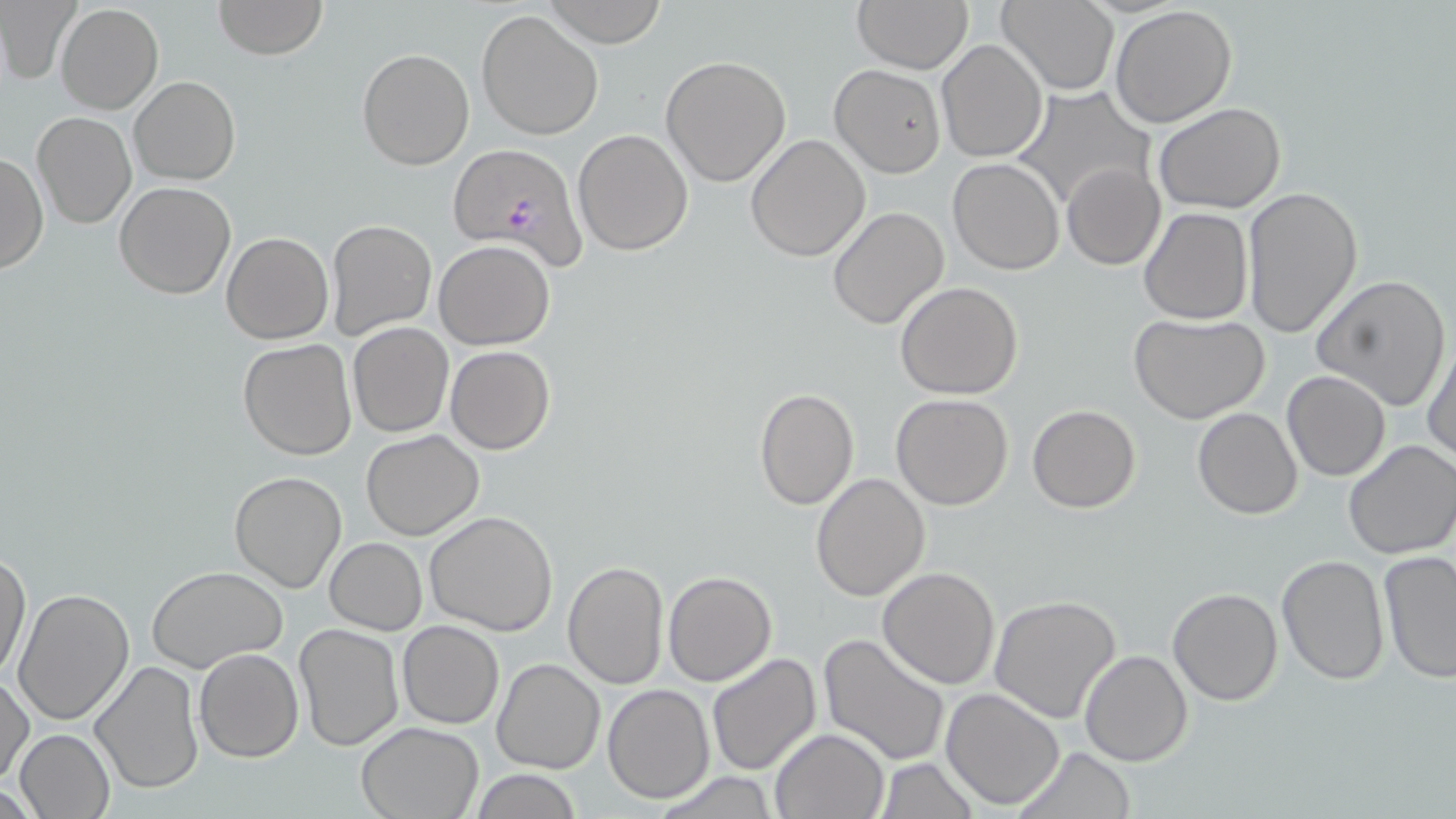 Approximate bounding boxes as (x1, y1, x2, y2) in pixels. Uninfected red blood cell locations: (0, 0, 80, 85), (212, 0, 327, 59), (543, 0, 669, 47), (852, 0, 974, 72), (997, 0, 1120, 94), (55, 3, 163, 114), (1109, 6, 1238, 128), (476, 8, 605, 141), (936, 39, 1046, 164), (356, 48, 474, 170), (660, 55, 792, 188), (829, 65, 947, 177), (130, 76, 240, 185), (1014, 84, 1157, 211), (1154, 102, 1286, 213), (31, 111, 136, 229), (573, 129, 694, 255), (746, 134, 872, 262), (1, 150, 47, 274), (947, 158, 1066, 275), (1063, 161, 1165, 270), (114, 182, 236, 299), (1240, 185, 1363, 340), (827, 205, 950, 330), (1138, 207, 1253, 326), (325, 219, 437, 341), (222, 232, 333, 344), (433, 240, 557, 350), (1312, 274, 1451, 412), (896, 281, 1023, 401), (1128, 313, 1272, 425), (349, 322, 455, 437), (1424, 337, 1456, 467), (238, 339, 357, 460), (446, 345, 555, 454), (1281, 369, 1390, 481), (753, 388, 859, 511), (891, 393, 1015, 510), (1027, 405, 1142, 513), (1192, 406, 1302, 519), (360, 429, 485, 539), (1343, 438, 1456, 560), (228, 470, 347, 593), (810, 472, 930, 601), (424, 511, 558, 637), (324, 538, 426, 634), (0, 550, 31, 683), (1375, 550, 1456, 683), (1276, 553, 1391, 686), (563, 561, 669, 688), (147, 566, 288, 675), (877, 566, 1001, 688), (663, 571, 777, 687), (1167, 586, 1283, 706), (12, 588, 135, 727), (989, 595, 1122, 725), (398, 621, 503, 729), (293, 624, 406, 753), (819, 630, 952, 765), (194, 649, 304, 763), (1079, 649, 1193, 766), (705, 651, 821, 776), (493, 658, 605, 774), (90, 659, 205, 797), (1, 673, 35, 785), (603, 684, 716, 803), (941, 687, 1067, 810), (356, 721, 483, 818), (769, 727, 890, 818), (13, 729, 116, 819), (1013, 745, 1137, 819), (877, 757, 978, 819), (468, 771, 584, 818), (654, 772, 781, 817). Plasmodium falciparum-infected red blood cell locations: (446, 143, 586, 268). Slide-level diagnosis: Plasmodium falciparum. One field of a larger specimen. Light microscopy. Captured at 1000x magnification. Image is 1456×819 pixels. Thin blood film. May-Grünwald-Giemsa-stained preparation.